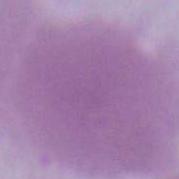
Summary:
  - Identification: red blood cell
  - Modality: photomicrograph
  - Magnification: 1000x